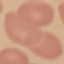
malaria_status: uninfected
stain: Giemsa
image_type: automatically extracted cell patch, resized to 64 × 64 pixels
preparation: thin blood film
capture: smartphone camera at the microscope eyepiece